Assess this cell for malaria.
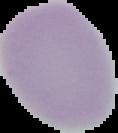
It is uninfected.

Image is 118×133 pixels. Segmented cell region on a black background. From a thin blood smear.